Locate every Plasmodium parasite by life-cycle stage, and every leukocyte.
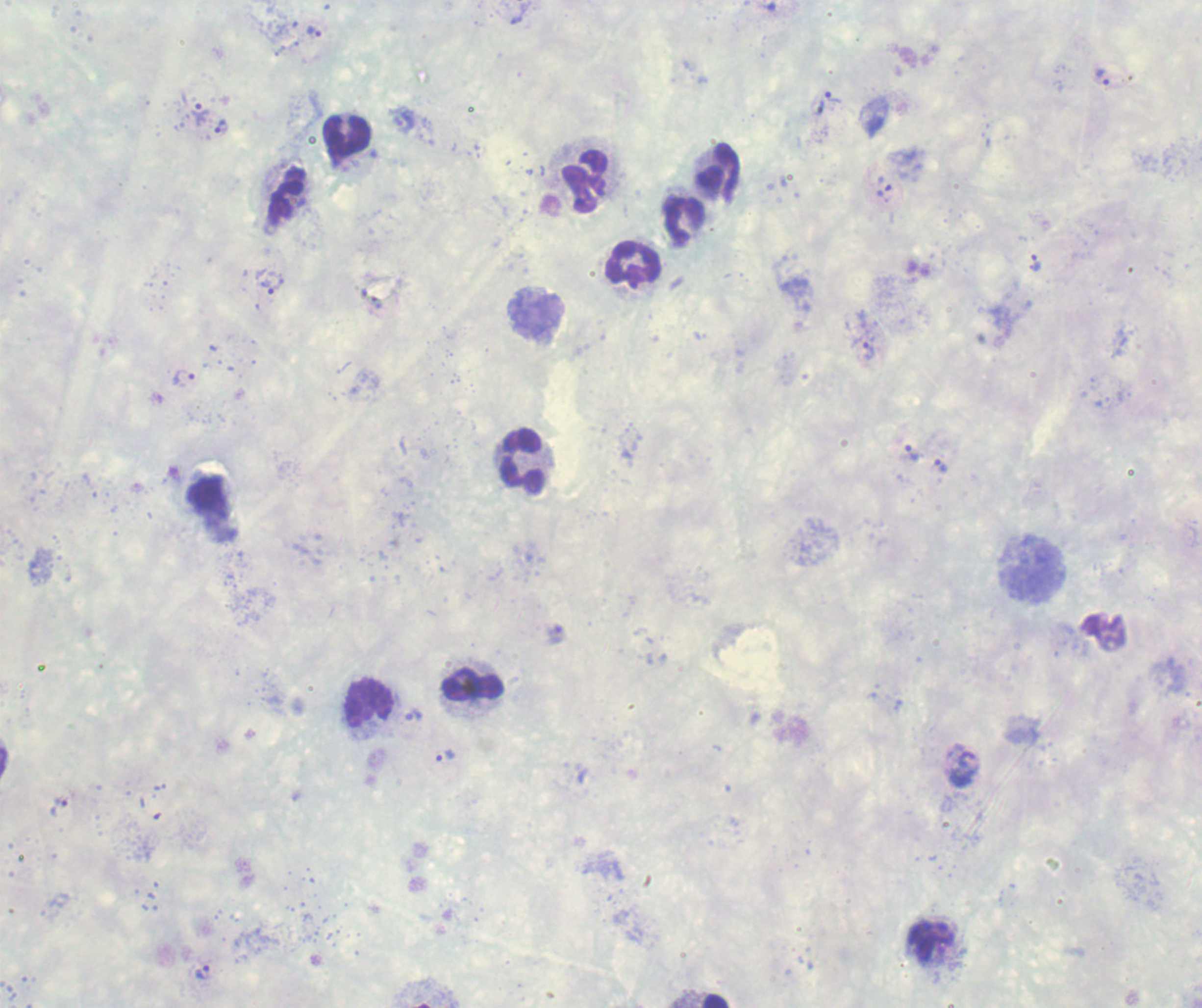
Approximate centers as {x, y} in pixels.
Trophozoites: {314, 32}, {1101, 77}, {835, 97}, {199, 112}, {221, 127}, {885, 189}, {1035, 262}, {272, 283}, {868, 351}, {185, 377}, {912, 453}, {940, 464}, {414, 716}, {444, 756}, {60, 807}, {203, 972}.
No schizont or gametocyte forms observed.
Leukocytes: {347, 137}, {720, 172}, {584, 181}, {288, 195}, {684, 221}, {634, 265}, {521, 461}, {473, 685}, {366, 703}, {713, 1000}.

preparation = thick smear of blood
field of view = single
context = previously used in a real diagnosis
stain = Romanowsky
magnification = 100x
background quality = poor
image size = 1202×1008 pixels